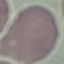
Summary:
  - Malaria status: uninfected
  - Stain: Giemsa
  - Image type: cell patch, automatically extracted from a larger field of view and resized to 64 × 64 pixels
  - Capture: smartphone camera at the microscope eyepiece
  - Preparation: thin blood film